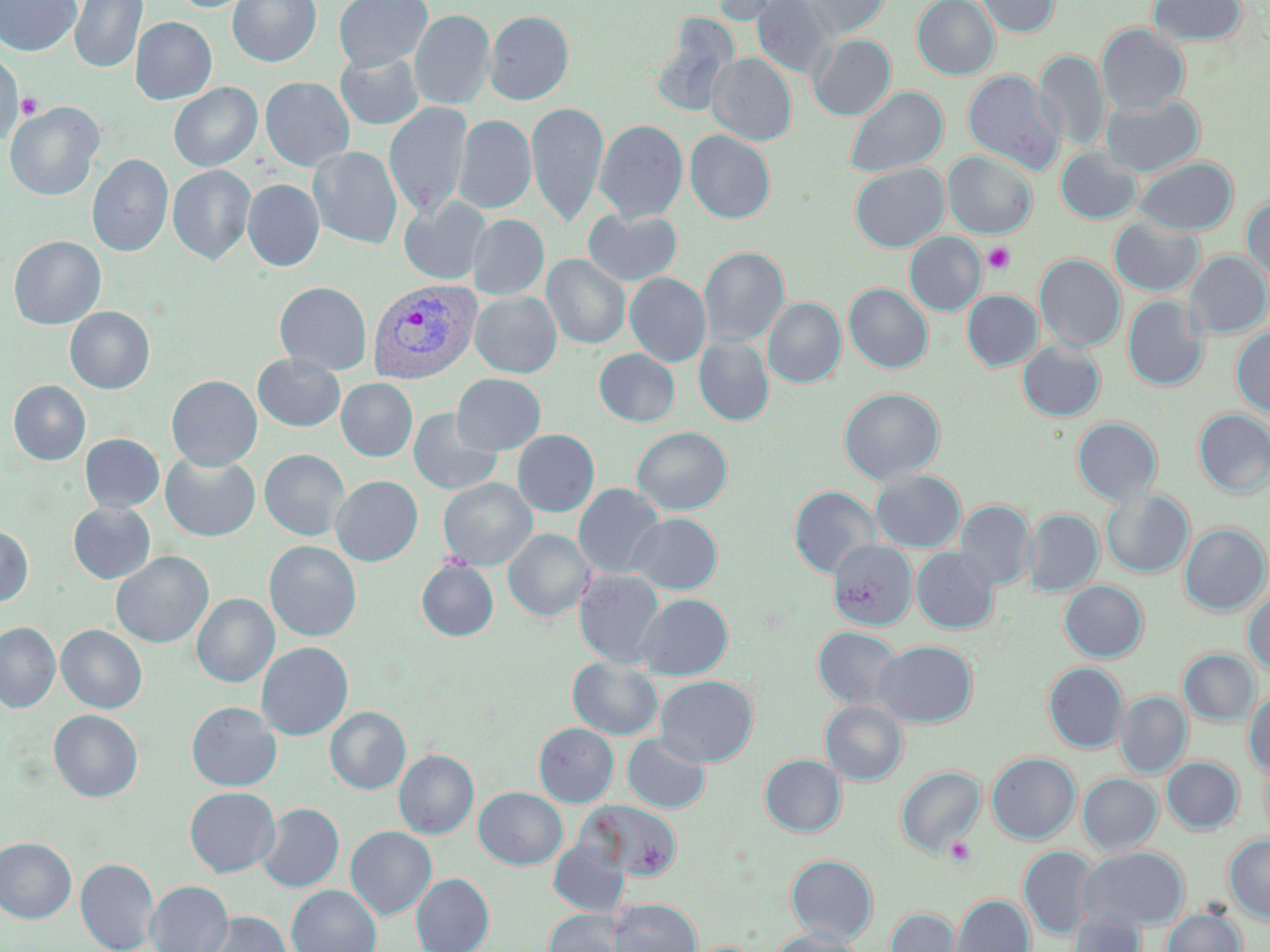
Approximate bounding boxes as named x1/y1/x2/y2 corners in pixels. Plasmodium vivax-infected red blood cell locations: (x1=368, y1=278, x2=482, y2=384). Platelet locations: (x1=5, y1=77, x2=39, y2=124), (x1=15, y1=91, x2=43, y2=119), (x1=983, y1=242, x2=1015, y2=274), (x1=943, y1=836, x2=977, y2=868). Uninfected red blood cell locations: (x1=0, y1=0, x2=82, y2=57), (x1=69, y1=0, x2=147, y2=73), (x1=170, y1=0, x2=258, y2=13), (x1=228, y1=0, x2=321, y2=67), (x1=333, y1=0, x2=432, y2=72), (x1=710, y1=0, x2=795, y2=26), (x1=752, y1=0, x2=836, y2=81), (x1=802, y1=0, x2=891, y2=40), (x1=912, y1=0, x2=999, y2=80), (x1=976, y1=0, x2=1060, y2=37), (x1=1147, y1=0, x2=1247, y2=47), (x1=409, y1=9, x2=494, y2=110), (x1=485, y1=10, x2=574, y2=105), (x1=650, y1=16, x2=738, y2=118), (x1=131, y1=17, x2=217, y2=104), (x1=1095, y1=24, x2=1190, y2=116), (x1=808, y1=34, x2=895, y2=120), (x1=1034, y1=50, x2=1111, y2=151), (x1=0, y1=51, x2=24, y2=144), (x1=335, y1=51, x2=424, y2=130), (x1=707, y1=53, x2=796, y2=146), (x1=963, y1=70, x2=1064, y2=174), (x1=260, y1=76, x2=355, y2=172), (x1=169, y1=83, x2=262, y2=172), (x1=845, y1=86, x2=948, y2=178), (x1=1101, y1=95, x2=1204, y2=177), (x1=526, y1=101, x2=608, y2=228), (x1=4, y1=102, x2=104, y2=201), (x1=384, y1=102, x2=473, y2=221), (x1=454, y1=114, x2=536, y2=214), (x1=594, y1=119, x2=688, y2=224), (x1=685, y1=130, x2=775, y2=223), (x1=309, y1=146, x2=403, y2=250), (x1=1055, y1=148, x2=1142, y2=224), (x1=942, y1=151, x2=1037, y2=238), (x1=87, y1=154, x2=173, y2=257), (x1=1133, y1=156, x2=1237, y2=234), (x1=850, y1=163, x2=949, y2=252), (x1=168, y1=164, x2=256, y2=266), (x1=242, y1=179, x2=324, y2=272), (x1=399, y1=196, x2=491, y2=285), (x1=1242, y1=196, x2=1270, y2=282), (x1=584, y1=208, x2=683, y2=286), (x1=468, y1=214, x2=549, y2=301), (x1=1109, y1=218, x2=1204, y2=296), (x1=904, y1=232, x2=986, y2=316), (x1=9, y1=235, x2=106, y2=330), (x1=699, y1=246, x2=789, y2=347), (x1=1184, y1=251, x2=1270, y2=338), (x1=542, y1=254, x2=630, y2=349), (x1=1035, y1=254, x2=1125, y2=352), (x1=624, y1=272, x2=711, y2=367), (x1=274, y1=281, x2=372, y2=375), (x1=844, y1=283, x2=933, y2=373), (x1=962, y1=290, x2=1043, y2=371), (x1=470, y1=291, x2=562, y2=377), (x1=1123, y1=295, x2=1209, y2=391), (x1=763, y1=297, x2=845, y2=388), (x1=65, y1=306, x2=155, y2=394), (x1=1231, y1=327, x2=1270, y2=416), (x1=693, y1=336, x2=774, y2=426), (x1=1017, y1=340, x2=1105, y2=421), (x1=594, y1=348, x2=680, y2=426), (x1=253, y1=353, x2=345, y2=432), (x1=452, y1=374, x2=546, y2=455), (x1=167, y1=375, x2=262, y2=471), (x1=336, y1=378, x2=418, y2=462), (x1=8, y1=380, x2=90, y2=466), (x1=839, y1=387, x2=945, y2=485), (x1=408, y1=408, x2=503, y2=496), (x1=1194, y1=409, x2=1270, y2=497), (x1=1072, y1=417, x2=1163, y2=505), (x1=632, y1=426, x2=732, y2=515), (x1=512, y1=429, x2=599, y2=517), (x1=80, y1=434, x2=164, y2=512), (x1=259, y1=449, x2=350, y2=541), (x1=160, y1=453, x2=260, y2=542), (x1=870, y1=469, x2=966, y2=552), (x1=331, y1=475, x2=423, y2=566), (x1=438, y1=477, x2=537, y2=570), (x1=573, y1=483, x2=665, y2=579), (x1=789, y1=485, x2=881, y2=578), (x1=1101, y1=489, x2=1194, y2=578), (x1=955, y1=499, x2=1035, y2=591), (x1=68, y1=502, x2=156, y2=583), (x1=1022, y1=509, x2=1103, y2=596), (x1=629, y1=513, x2=722, y2=594), (x1=1180, y1=522, x2=1269, y2=615), (x1=0, y1=525, x2=33, y2=607), (x1=503, y1=528, x2=595, y2=622), (x1=828, y1=539, x2=918, y2=630), (x1=264, y1=540, x2=362, y2=641), (x1=911, y1=547, x2=999, y2=634), (x1=111, y1=551, x2=214, y2=648), (x1=416, y1=559, x2=498, y2=641), (x1=574, y1=568, x2=665, y2=668), (x1=1059, y1=581, x2=1148, y2=662), (x1=1243, y1=589, x2=1270, y2=677), (x1=192, y1=593, x2=279, y2=688), (x1=637, y1=593, x2=733, y2=680), (x1=0, y1=621, x2=60, y2=713), (x1=56, y1=625, x2=147, y2=714), (x1=812, y1=626, x2=904, y2=710), (x1=872, y1=640, x2=977, y2=727), (x1=256, y1=642, x2=353, y2=740), (x1=1179, y1=649, x2=1259, y2=726), (x1=568, y1=657, x2=663, y2=739), (x1=1043, y1=662, x2=1128, y2=752), (x1=655, y1=675, x2=758, y2=767), (x1=1244, y1=688, x2=1270, y2=778), (x1=1115, y1=692, x2=1192, y2=777), (x1=820, y1=699, x2=908, y2=785), (x1=186, y1=702, x2=281, y2=791), (x1=325, y1=706, x2=410, y2=794), (x1=49, y1=710, x2=143, y2=802), (x1=534, y1=723, x2=619, y2=806), (x1=623, y1=733, x2=711, y2=813), (x1=393, y1=749, x2=479, y2=839), (x1=987, y1=753, x2=1081, y2=843), (x1=760, y1=754, x2=846, y2=837), (x1=1162, y1=757, x2=1244, y2=834), (x1=897, y1=763, x2=1081, y2=851), (x1=896, y1=766, x2=985, y2=857), (x1=1078, y1=773, x2=1162, y2=855), (x1=184, y1=786, x2=280, y2=877), (x1=473, y1=787, x2=567, y2=869), (x1=581, y1=800, x2=682, y2=882), (x1=256, y1=803, x2=344, y2=892), (x1=345, y1=826, x2=436, y2=920), (x1=1224, y1=834, x2=1270, y2=924), (x1=0, y1=837, x2=76, y2=923), (x1=549, y1=837, x2=629, y2=916), (x1=1019, y1=846, x2=1097, y2=939), (x1=1078, y1=846, x2=1189, y2=930), (x1=786, y1=854, x2=877, y2=942), (x1=76, y1=858, x2=160, y2=952), (x1=411, y1=873, x2=494, y2=952), (x1=146, y1=880, x2=233, y2=952), (x1=287, y1=885, x2=381, y2=952), (x1=949, y1=894, x2=1034, y2=952), (x1=609, y1=898, x2=701, y2=952), (x1=885, y1=907, x2=960, y2=952), (x1=543, y1=908, x2=628, y2=952), (x1=1162, y1=908, x2=1246, y2=952), (x1=201, y1=911, x2=292, y2=952), (x1=1067, y1=911, x2=1146, y2=952), (x1=767, y1=929, x2=864, y2=952). Slide-level diagnosis: Plasmodium vivax. Single field of view. Light microscopy. Image is 1270×952 pixels. May-Grünwald-Giemsa-stained preparation. Captured at 1000x magnification. Thin blood smear.